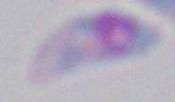

{
  "modality": "micrograph",
  "magnification": "1000x",
  "identification": "Toxoplasma gondii"
}